Point out every Plasmodium parasite.
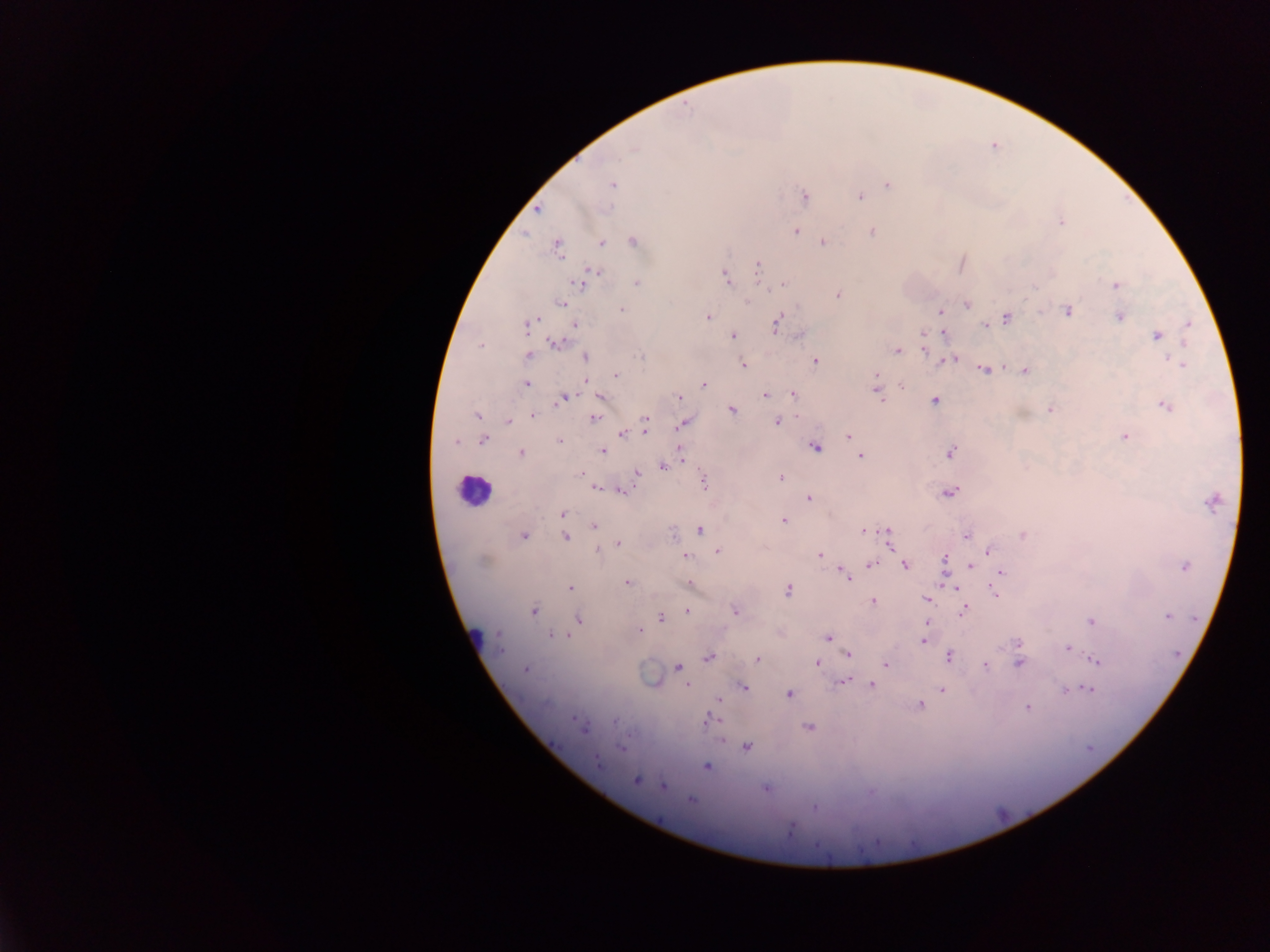

Approximate centers as [x, y] in pixels.
Plasmodium parasites: [633, 149], [612, 185], [887, 185], [804, 194], [861, 196], [537, 208], [1060, 223], [871, 231], [797, 232], [525, 237], [633, 240], [601, 242], [823, 243], [559, 247], [758, 266], [724, 276], [579, 282], [635, 282], [1116, 285], [773, 288], [836, 294], [563, 303], [968, 305], [622, 309], [1067, 311], [939, 312], [708, 316], [1006, 317], [1119, 317], [1189, 321], [775, 322], [576, 324], [528, 326], [985, 327], [943, 331], [733, 336], [1156, 337], [1185, 342], [555, 344], [897, 351], [528, 355], [586, 356], [639, 357], [1170, 359], [815, 360], [943, 360], [955, 360], [741, 364], [1183, 365], [1004, 367], [984, 370], [1024, 370], [615, 375], [876, 377], [903, 383], [527, 385], [703, 386], [766, 394], [792, 394], [879, 395], [564, 396], [598, 396], [678, 398], [560, 401], [934, 401], [1166, 404], [1051, 408], [732, 410], [477, 415], [532, 416], [798, 416], [645, 418], [593, 419], [683, 422], [776, 422], [508, 423], [646, 433], [622, 434], [847, 436], [1123, 437], [482, 438], [558, 440], [453, 441], [816, 447], [603, 450], [680, 451], [521, 452], [949, 452], [861, 455], [686, 461], [662, 466], [579, 473], [636, 474], [782, 478], [703, 482], [594, 488], [622, 491], [949, 494], [807, 497], [1209, 505], [561, 513], [783, 519], [593, 528], [701, 531], [862, 531], [888, 531], [524, 535], [566, 536], [965, 536], [1022, 536], [617, 543], [889, 547], [717, 550], [987, 550], [598, 551], [820, 554], [686, 556], [945, 559], [484, 561], [870, 565], [905, 566], [1184, 566], [971, 567], [1001, 572], [842, 574], [939, 577], [628, 582], [689, 583], [570, 588], [956, 590], [787, 591], [995, 595], [874, 600], [925, 600], [964, 610], [534, 611], [686, 611], [734, 611], [1167, 616], [660, 618], [578, 619], [1090, 620], [639, 630], [496, 633], [550, 633], [563, 636], [569, 637], [828, 639], [924, 641], [1019, 643], [1067, 647], [499, 651], [847, 654], [708, 657], [756, 659], [1096, 660], [817, 662], [884, 664], [1020, 665], [676, 667], [985, 667], [526, 671], [844, 680], [872, 685], [685, 686], [745, 688], [1089, 689], [941, 690], [1067, 692], [787, 693], [719, 700], [922, 705], [1025, 708], [714, 718], [616, 719], [575, 720], [808, 727], [582, 730], [747, 748], [620, 749], [596, 761], [707, 766], [636, 781], [663, 786], [691, 802], [812, 807], [791, 828], [817, 844].

image size = 1270×952 pixels
field of view = single
capture = mobile-phone photograph through a microscope
country = Ghana
leukocyte locations = approximate centers as [x, y] in pixels: [478, 488]
preparation = thick blood smear